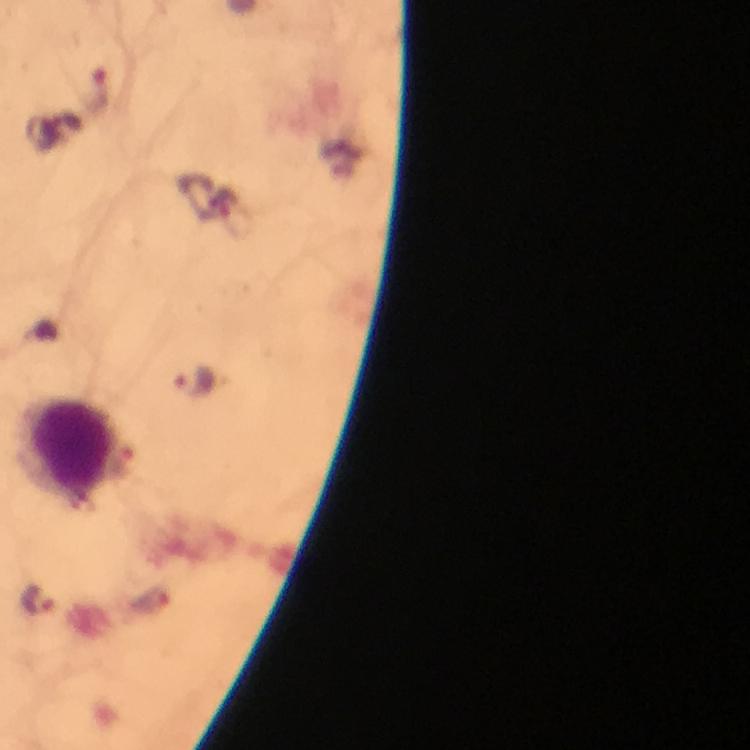
Approximate centers as [x, y] in pixels.
Summary:
  - Plasmodium parasite locations: [98, 94], [194, 382], [39, 600]
  - Leukocyte locations: [70, 453]
  - Context: from a malaria diagnostic workup
  - Image size: 750×750 pixels
  - Preparation: thick blood smear
  - Cropped from: one field of view
  - Capture: smartphone photograph through a microscope
  - Immersion oil: applied
  - Magnification: 100x
  - Stain: Giemsa